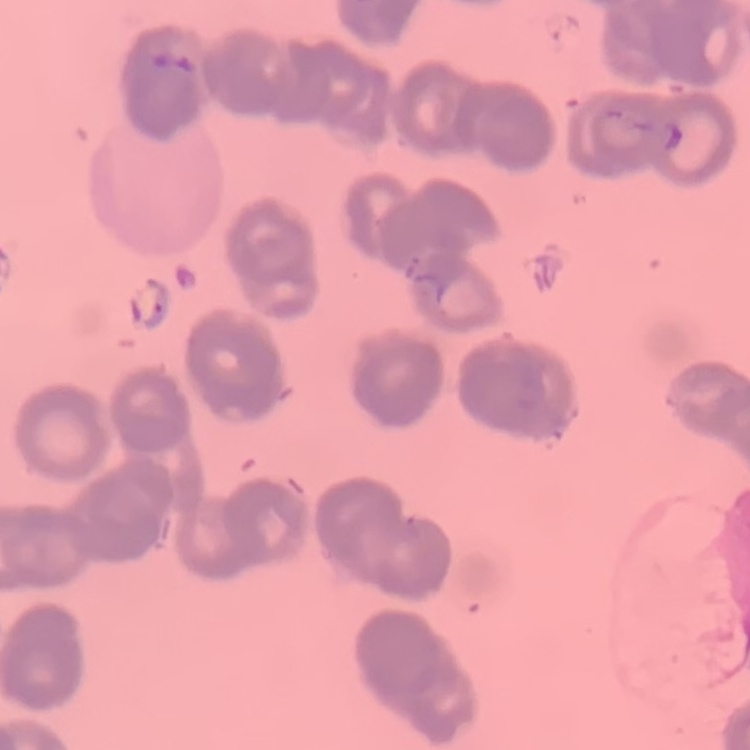

Summary:
  - Red blood cell morphology: rouleaux formation
  - Image type: square crop of a larger photomicrograph
  - Preparation: thin peripheral smear
  - Stain: Field's or Giemsa